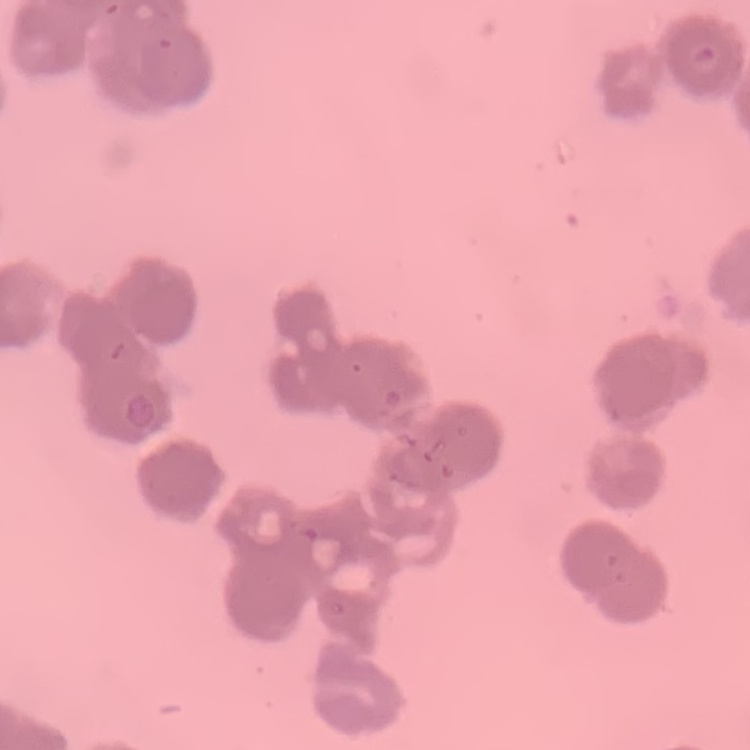 The erythrocytes exhibit rouleaux formation. Square crop of a larger photomicrograph. Stained with either Field's or Giemsa. Thin peripheral smear.